Comment on the morphology of the erythrocytes.
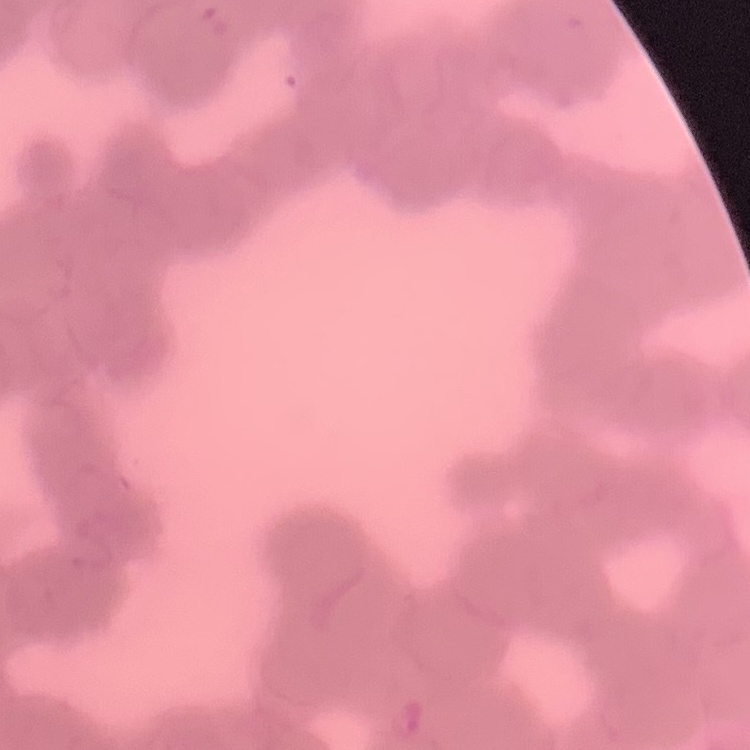
They show rouleaux formation.

One tile cut from a larger photomicrograph. Stained with either Field's or Giemsa. Thin blood smear.